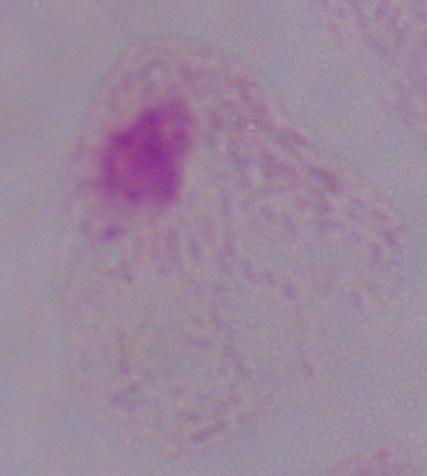

magnification = 1000x
modality = photomicrograph
identification = trichomonad